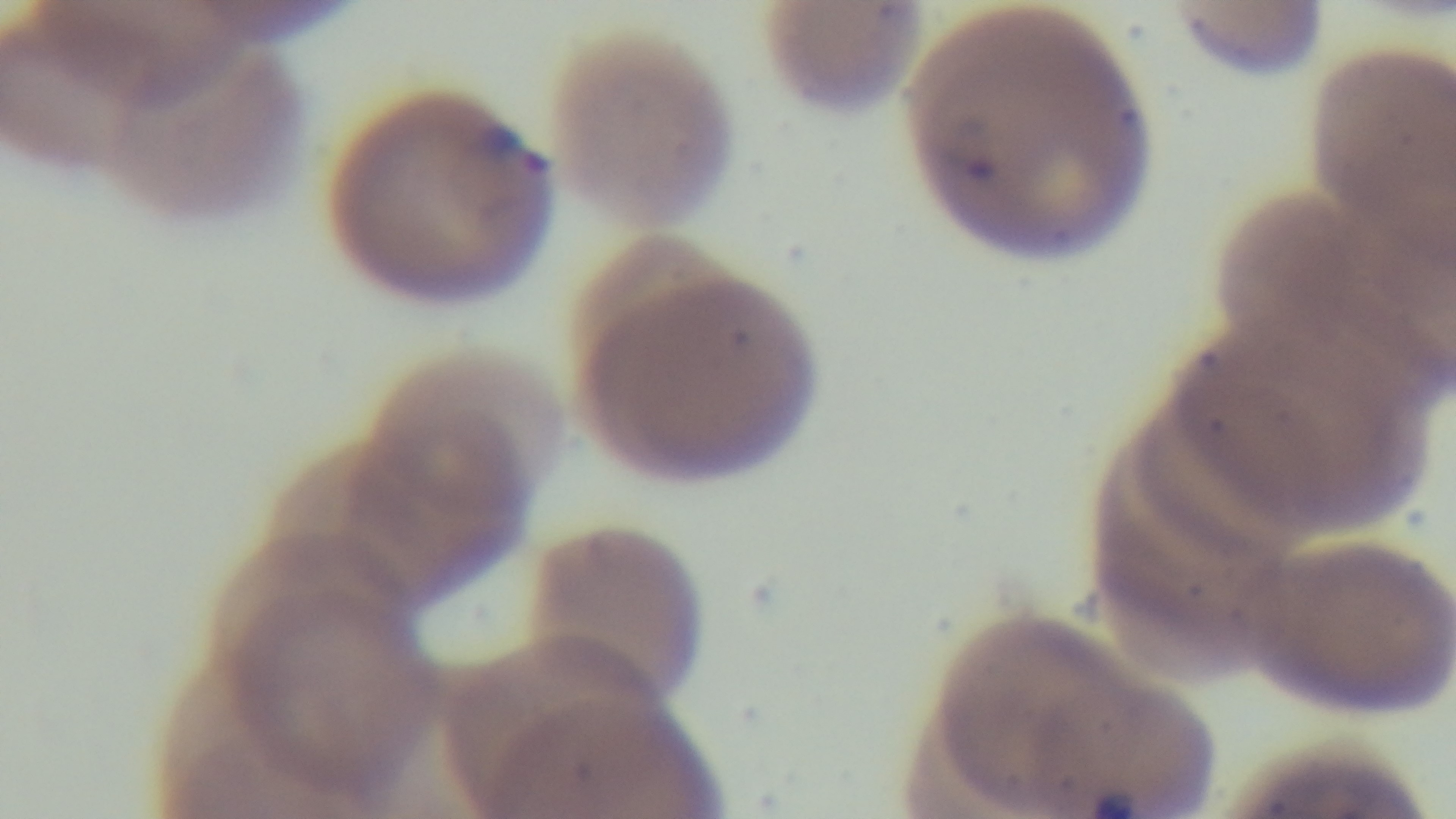 Malaria status: infected. Oil-immersion objective, 100x. Captured with a mounted 4K digital camera. Preparation: thin. Giemsa-stained. Photomicrograph. Single field of view.